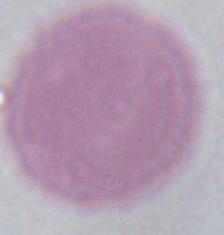

Photomicrograph. An erythrocyte is seen. Captured at 1000x magnification.